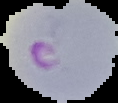
image_size: 118×103 pixels
preparation: thin blood film
image_type: segmented cell region on a black background
malaria_status: parasitized